Report the malaria status of this cell.
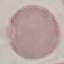

Uninfected.

Automatically extracted cell patch, resized to 64 × 64 pixels. Thin blood smear. Giemsa stain. Acquired by smartphone through the microscope eyepiece.